Classify this cell by malaria status.
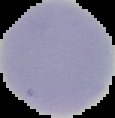
Uninfected.

Summary:
  - Image type: segmented cell region with the area outside set to black
  - Image size: 115×118 pixels
  - Preparation: thin blood smear